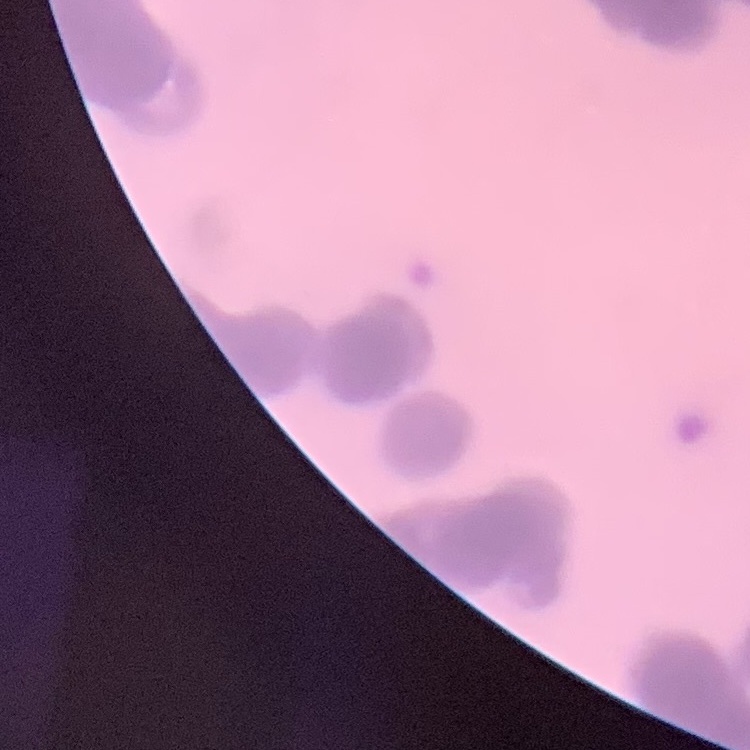
Summary:
  - Erythrocyte morphology: rouleaux formation
  - Preparation: thin blood film
  - Stain: Field's or Giemsa
  - Image type: square crop of a larger photomicrograph